Name the parasite shown.
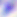
This is Toxoplasma gondii.

Summary:
  - Magnification: 400x
  - Modality: photomicrograph